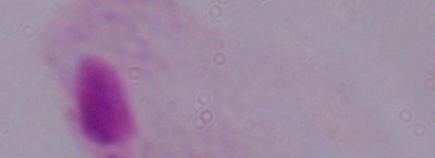

Summary:
  - Identification: trichomonad
  - Modality: photomicrograph
  - Magnification: 1000x